Name the parasite shown.
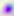

This is Toxoplasma gondii.

Summary:
  - Magnification: 400x
  - Modality: micrograph